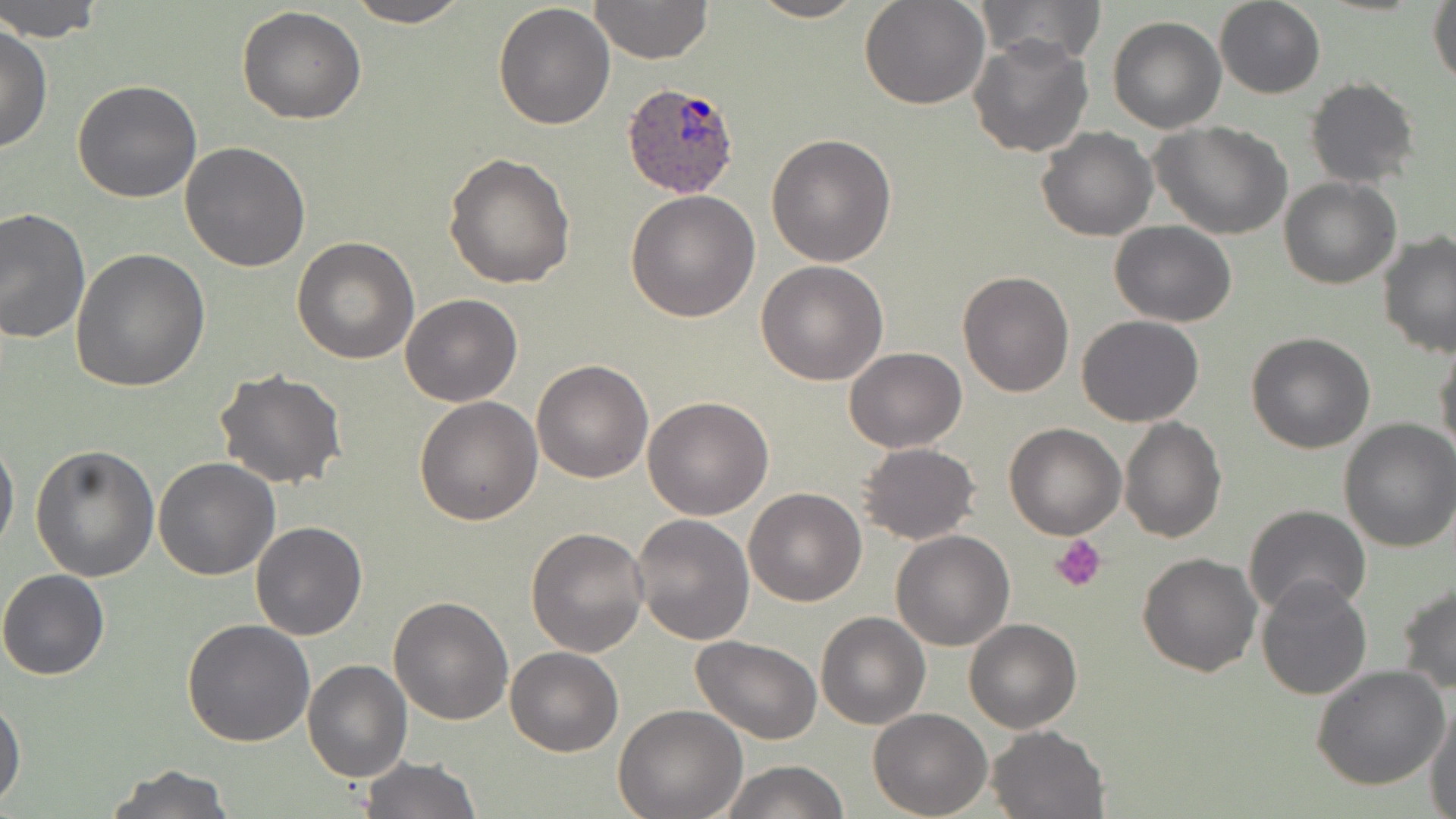

Approximate bounding boxes as (x1,y1)-(x2,y2) corner pairs in pixels. Plasmodium ovale-infected red blood cell locations: (620,82)-(742,200). Platelet locations: (1052,535)-(1105,591). Uninfected red blood cell locations: (1,0)-(105,42), (345,0)-(473,28), (589,0)-(713,65), (747,0)-(868,23), (860,0)-(988,109), (1213,0)-(1326,98), (1428,0)-(1456,90), (979,1)-(1106,64), (493,4)-(616,131), (237,6)-(367,125), (1107,17)-(1227,134), (0,26)-(52,155), (967,32)-(1093,157), (1304,77)-(1421,188), (73,80)-(203,202), (1151,122)-(1294,241), (1036,128)-(1158,242), (765,134)-(897,267), (180,140)-(311,271), (444,152)-(577,289), (1280,177)-(1401,289), (626,190)-(761,323), (0,207)-(91,343), (1109,220)-(1237,327), (1378,231)-(1456,358), (292,236)-(420,364), (71,249)-(211,395), (756,261)-(889,386), (955,269)-(1074,396), (400,293)-(523,406), (1076,314)-(1204,426), (1245,332)-(1376,454), (1433,340)-(1456,461), (842,347)-(966,452), (530,359)-(653,483), (214,368)-(348,490), (414,395)-(543,524), (643,396)-(773,520), (1119,415)-(1227,542), (1335,420)-(1456,553), (1004,421)-(1127,539), (0,435)-(19,557), (31,442)-(161,582), (856,442)-(981,545), (152,456)-(280,580), (743,488)-(868,606), (1242,504)-(1370,620), (630,514)-(755,646), (250,521)-(368,640), (526,527)-(649,657), (891,529)-(1016,650), (1137,551)-(1262,677), (0,569)-(109,681), (1255,576)-(1373,700), (1396,581)-(1456,694), (387,595)-(513,724), (815,611)-(931,729), (181,619)-(315,748), (964,619)-(1082,734), (690,635)-(822,744), (505,646)-(622,757), (302,659)-(413,783), (1311,666)-(1451,790), (1,696)-(25,806), (1426,700)-(1456,818), (612,703)-(747,818), (868,708)-(993,818), (987,724)-(1109,818), (360,756)-(481,819), (721,759)-(848,819), (102,764)-(236,818). Slide-level diagnosis: Plasmodium ovale. May-Grünwald-Giemsa stain. 1000x magnification. Optical microscopy. Image is 1456×819 pixels. Single field of view. Thin blood smear.